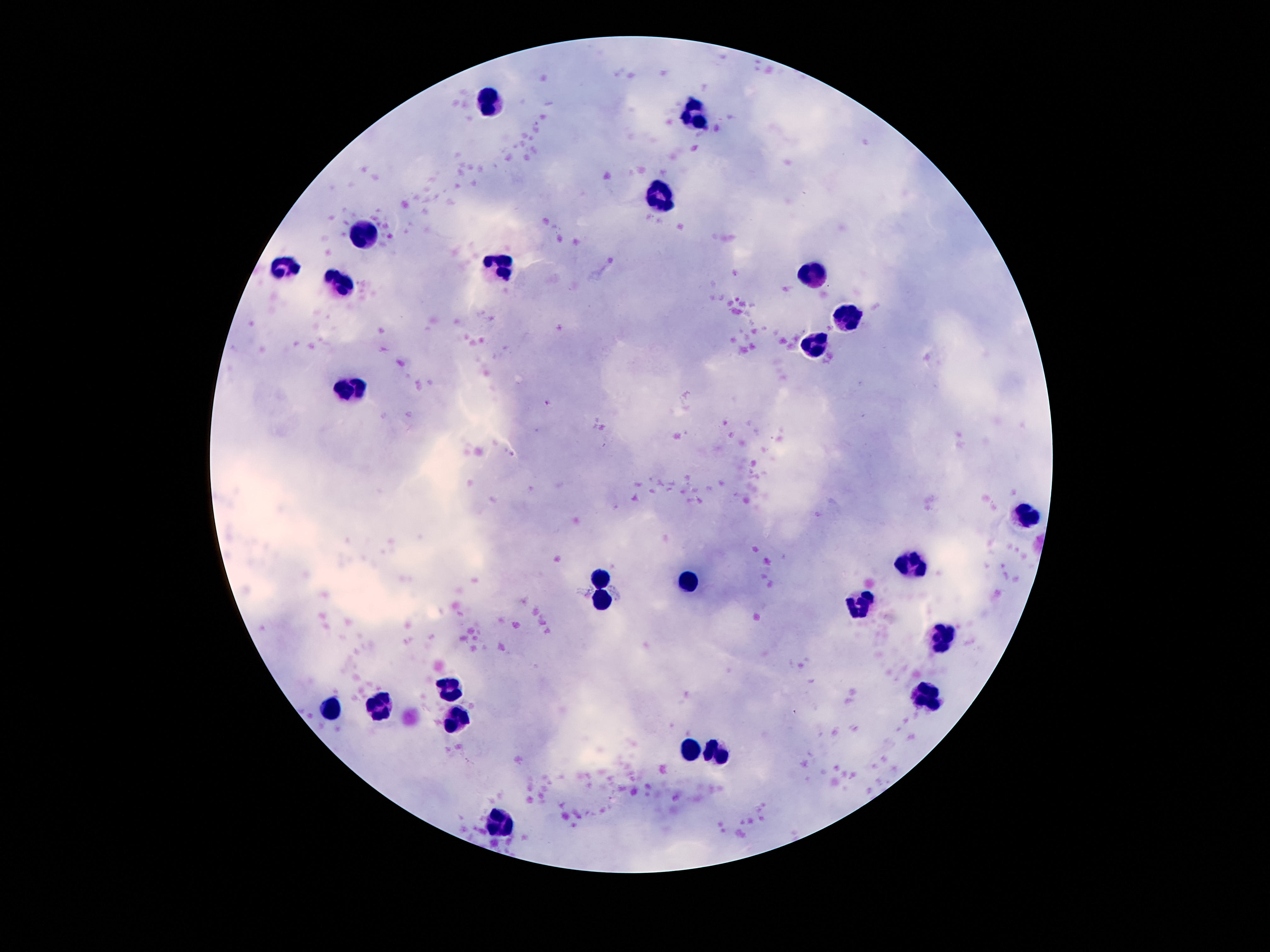
{
  "leukocyte_locations": "approximate object centers, in pixels from the top-left corner: (x=492, y=99), (x=693, y=115), (x=660, y=197), (x=364, y=232), (x=283, y=262), (x=497, y=269), (x=812, y=277), (x=338, y=285), (x=850, y=316), (x=815, y=346), (x=355, y=388), (x=1027, y=515), (x=912, y=563), (x=600, y=581), (x=691, y=581), (x=604, y=597), (x=863, y=602), (x=942, y=641), (x=450, y=682), (x=928, y=698), (x=380, y=702), (x=332, y=707), (x=457, y=714), (x=688, y=750), (x=716, y=756), (x=501, y=821)",
  "patient_malaria_status": "negative",
  "field_of_view": "single",
  "image_size": "1270×952 pixels",
  "preparation": "thick blood film",
  "magnification": "100x",
  "capture": "smartphone camera through the microscope eyepiece",
  "stain": "Giemsa"
}